Give the preparation type.
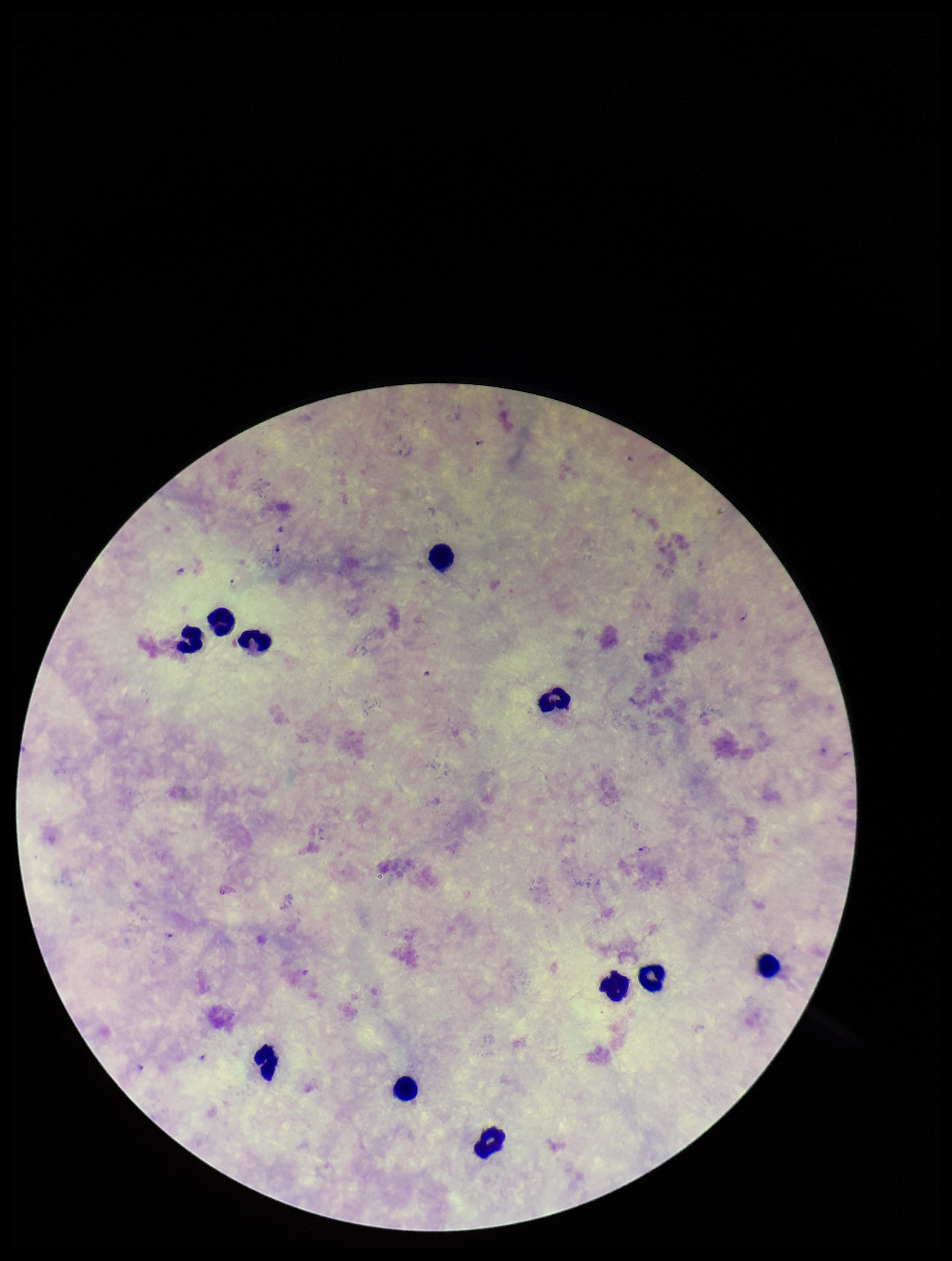
A thick smear.

Plasmodium parasites: detected. Leukocyte count: 11. Image is 952×1261 pixels. Patient malaria status: positive. Species reported for this patient: Plasmodium falciparum. Photographed through the microscope eyepiece with a smartphone camera. Single field of view. Stained with Giemsa. Parasite count: 2.